Report the malaria status of this cell.
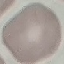

It is uninfected.

Summary:
  - Capture: smartphone through the microscope eyepiece
  - Stain: Giemsa
  - Preparation: thin smear
  - Image type: automatically extracted cell patch, resized to 64 × 64 pixels